Identify the parasite.
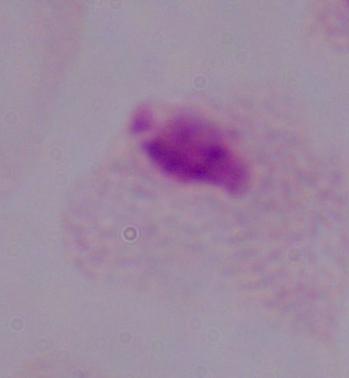

This is a trichomonad.

{
  "magnification": "1000x",
  "modality": "micrograph"
}